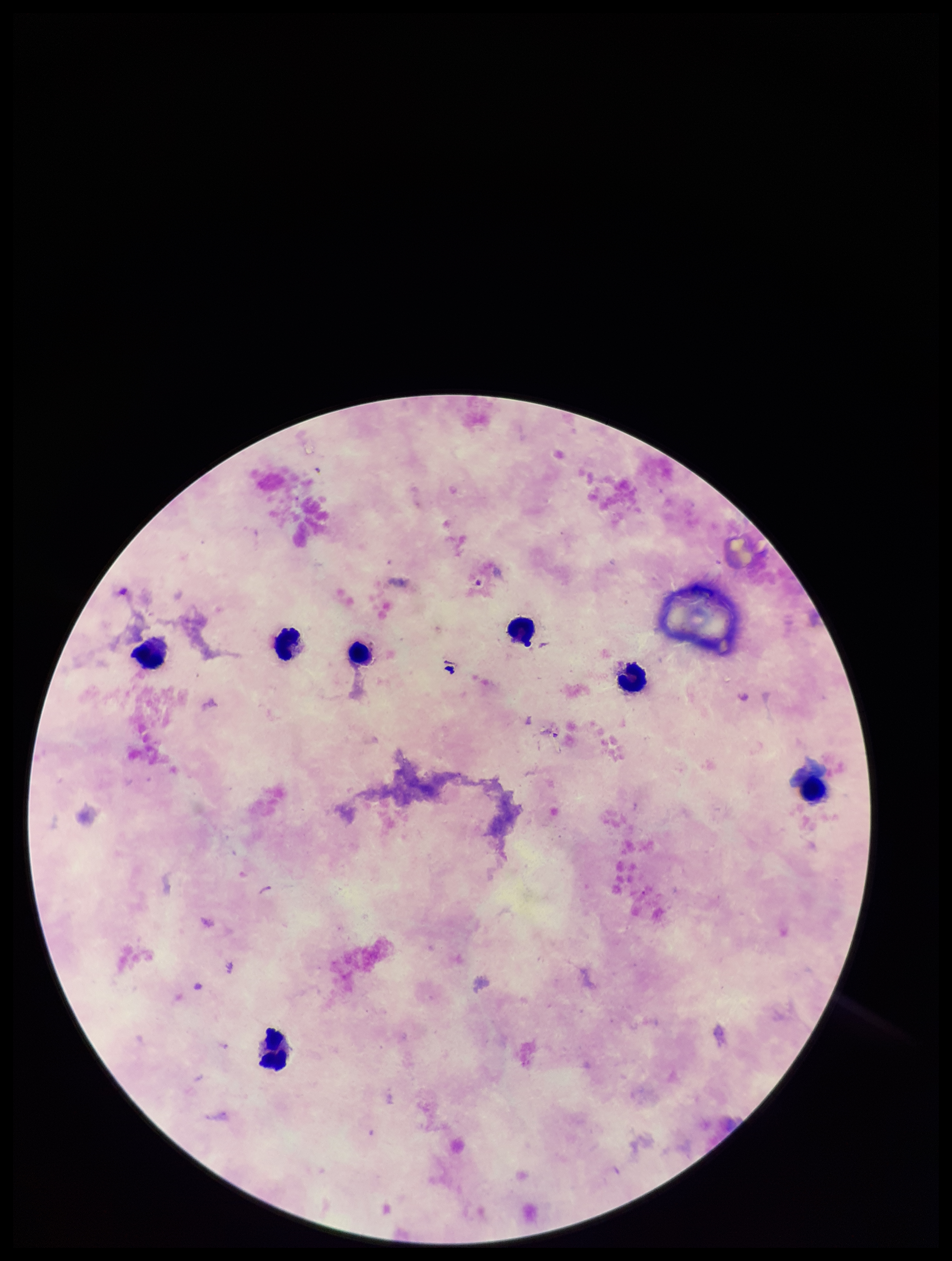
Summary:
  - Capture: smartphone photograph through the microscope eyepiece
  - Leukocyte count: 7
  - Field of view: one from this slide
  - Image size: 952×1261 pixels
  - Preparation: thick
  - Patient malaria status: negative
  - Parasite count: 0
  - Plasmodium parasites: none identified
  - Stain: Giemsa